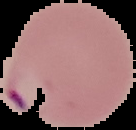
image type = segmented cell region with the area outside set to black
preparation = thin blood smear
malaria status = parasitized
image size = 136×130 pixels